Describe the morphology of the red blood cells.
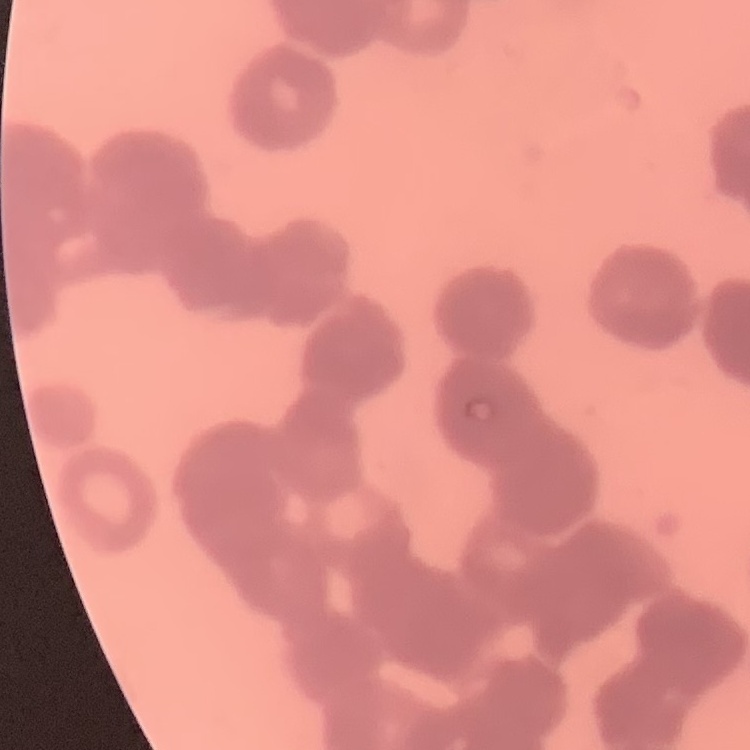
Rouleaux formation.

stain = Field's or Giemsa
image type = square crop of a larger photomicrograph
preparation = thin peripheral smear